Identify the parasite.
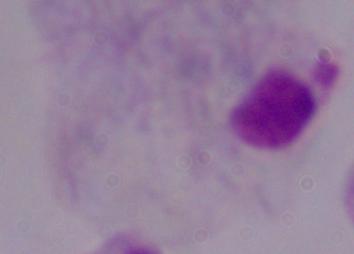

A trichomonad.

modality = photomicrograph
magnification = 1000x